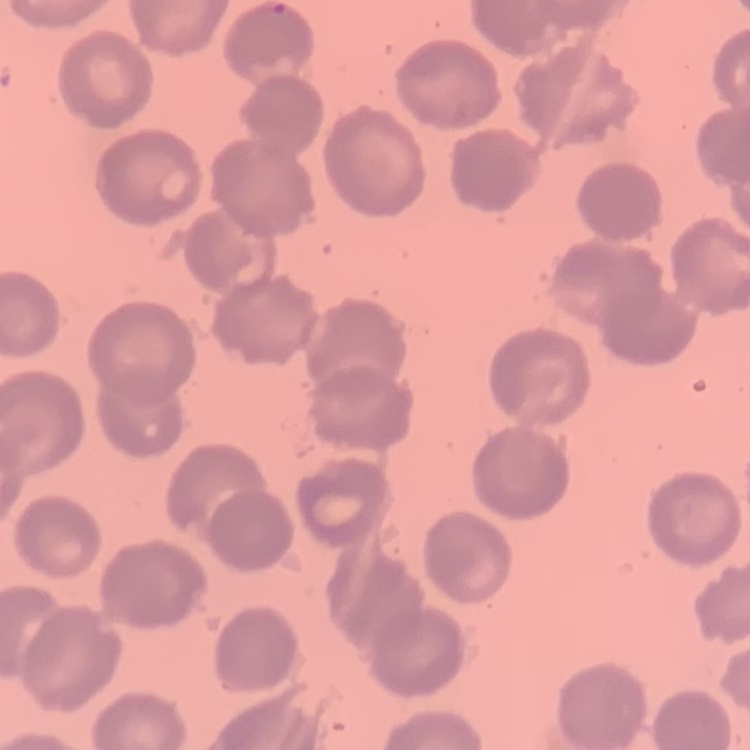

Summary:
  - Red blood cell morphology: no rouleaux formation
  - Image type: one tile cut from a larger photomicrograph
  - Preparation: thin blood film
  - Stain: Field's or Giemsa